Report the malaria status of this cell.
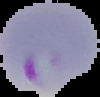
Parasitized.

preparation = thin blood film
image type = segmented cell region with the area outside set to black
image size = 100×97 pixels